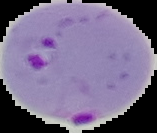

malaria status = parasitized
image size = 157×133 pixels
image type = segmented cell region with the area outside set to black
preparation = thin blood smear